Locate and identify every blood parasite.
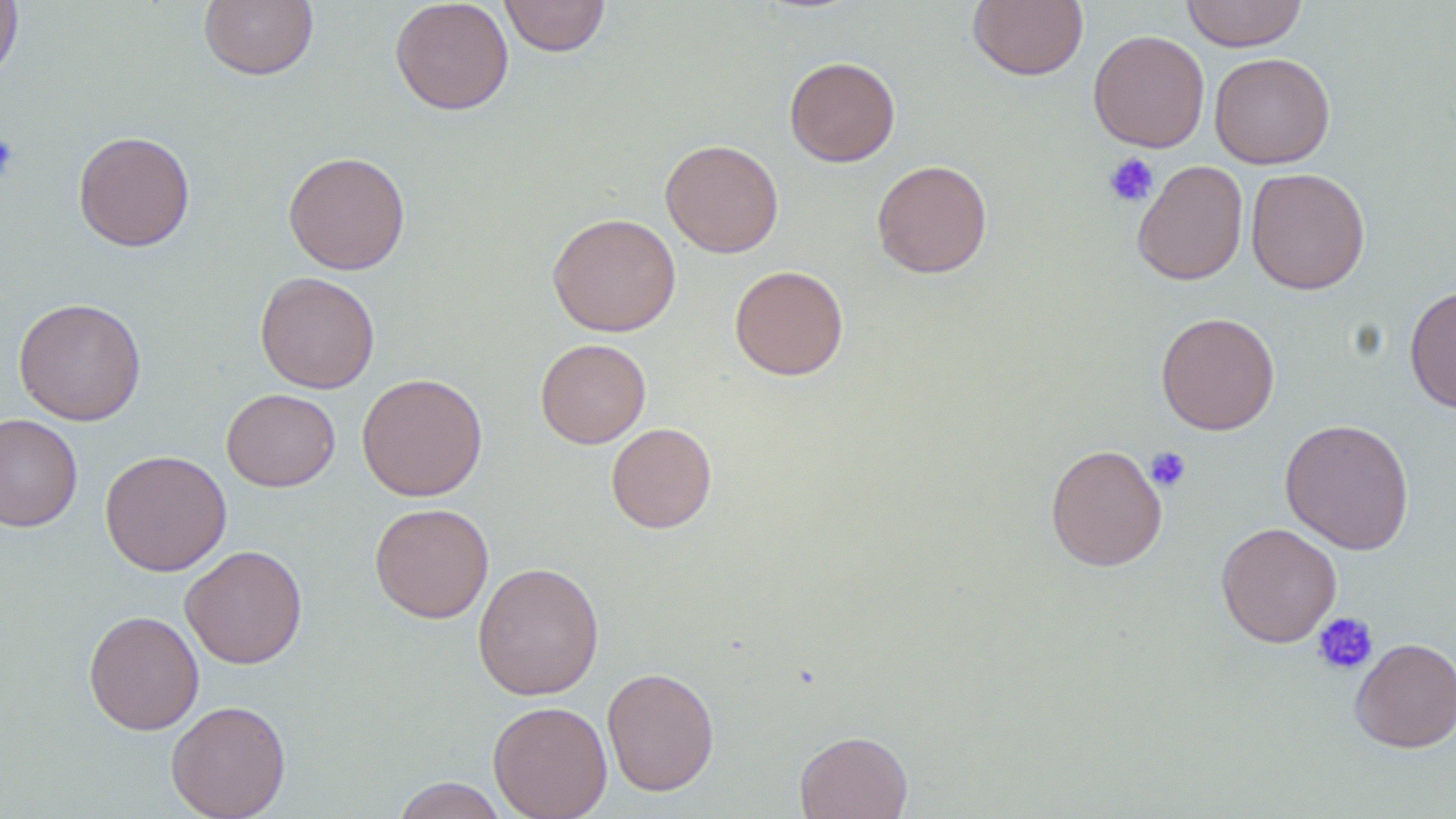

No blood parasites observed.

slide-level diagnosis = negative for blood parasites
magnification = 1000x
field of view = one of a larger specimen
uninfected red blood cell locations = approximate bounding boxes as named x1/y1/x2/y2 corners in pixels: (x1=199, y1=0, x2=319, y2=81), (x1=389, y1=0, x2=514, y2=115), (x1=499, y1=0, x2=611, y2=57), (x1=968, y1=0, x2=1088, y2=81), (x1=1180, y1=0, x2=1309, y2=52), (x1=0, y1=1, x2=23, y2=85), (x1=1088, y1=29, x2=1210, y2=152), (x1=1209, y1=52, x2=1335, y2=169), (x1=784, y1=56, x2=900, y2=167), (x1=73, y1=130, x2=196, y2=252), (x1=660, y1=139, x2=784, y2=258), (x1=283, y1=150, x2=410, y2=274), (x1=871, y1=159, x2=993, y2=278), (x1=1132, y1=160, x2=1249, y2=286), (x1=1245, y1=167, x2=1370, y2=294), (x1=547, y1=213, x2=682, y2=337), (x1=729, y1=265, x2=848, y2=381), (x1=255, y1=271, x2=380, y2=393), (x1=1404, y1=284, x2=1456, y2=414), (x1=14, y1=297, x2=146, y2=426), (x1=1155, y1=312, x2=1280, y2=435), (x1=535, y1=338, x2=651, y2=448), (x1=356, y1=372, x2=488, y2=502), (x1=222, y1=388, x2=340, y2=491), (x1=0, y1=413, x2=83, y2=532), (x1=1279, y1=418, x2=1415, y2=555), (x1=606, y1=422, x2=717, y2=533), (x1=1045, y1=443, x2=1167, y2=572), (x1=100, y1=449, x2=231, y2=577), (x1=369, y1=503, x2=494, y2=623), (x1=1216, y1=521, x2=1342, y2=648), (x1=180, y1=545, x2=308, y2=669), (x1=472, y1=561, x2=604, y2=701), (x1=83, y1=610, x2=204, y2=735), (x1=1349, y1=637, x2=1456, y2=753), (x1=602, y1=666, x2=720, y2=796), (x1=165, y1=700, x2=291, y2=818), (x1=488, y1=700, x2=613, y2=819), (x1=795, y1=730, x2=913, y2=819), (x1=391, y1=777, x2=510, y2=819)
platelet locations = approximate bounding boxes as named x1/y1/x2/y2 corners in pixels: (x1=0, y1=133, x2=20, y2=181), (x1=1103, y1=152, x2=1160, y2=208), (x1=1145, y1=446, x2=1192, y2=492), (x1=1311, y1=612, x2=1378, y2=676)
image size = 1456×819 pixels
modality = light microscopy
preparation = thin blood film
stain = May-Grünwald-Giemsa